Locate every leukocyte (white blood cell).
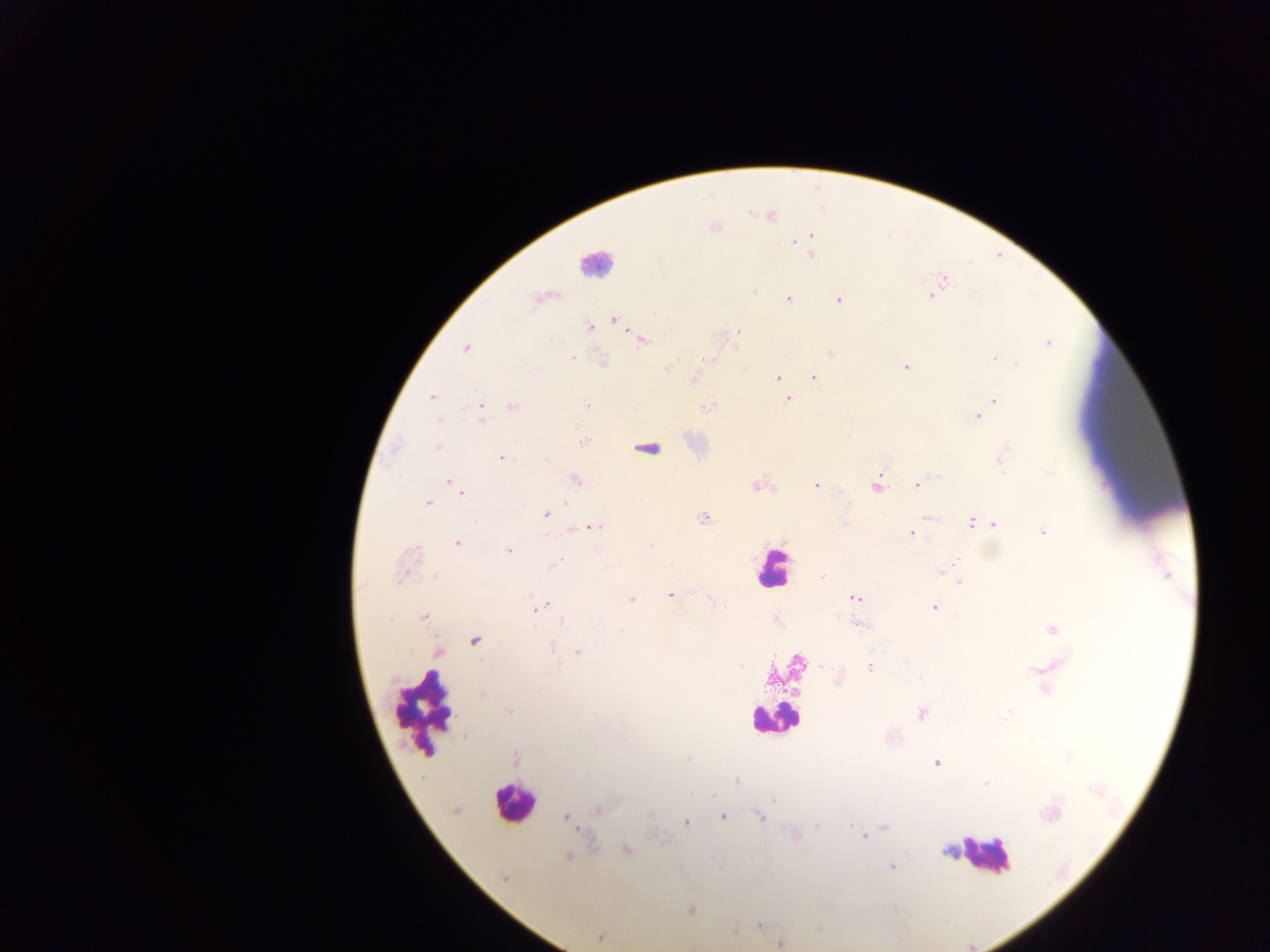

Approximate centers as x y in pixels.
Leukocytes: 595 263; 648 448; 773 569; 426 708; 773 718; 512 802; 984 854.

{
  "field_of_view": "single",
  "country": "Ghana",
  "malaria_parasite_locations": "approximate centers as x y in pixels: 771 216; 811 235; 802 239; 795 241; 812 255; 944 279; 754 291; 931 295; 788 298; 839 299; 615 321; 591 327; 738 331; 642 340; 1048 343; 465 349; 830 353; 572 358; 709 358; 993 358; 1017 364; 906 366; 666 369; 814 377; 777 378; 695 379; 431 397; 788 399; 996 400; 513 405; 587 405; 708 407; 482 415; 977 415; 439 420; 584 442; 438 446; 1001 457; 501 458; 1051 473; 575 479; 448 481; 876 484; 756 485; 816 485; 916 485; 462 493; 428 502; 566 503; 545 515; 927 517; 703 518; 972 521; 994 524; 845 525; 594 527; 1043 532; 912 533; 457 542; 651 545; 414 551; 508 551; 555 564; 941 571; 823 576; 948 576; 402 577; 960 582; 482 584; 670 594; 855 597; 632 600; 545 604; 934 607; 539 608; 724 608; 423 617; 562 621; 859 624; 1052 629; 475 640; 551 647; 578 652; 439 653; 871 668; 841 672; 481 695; 922 714; 1007 714; 515 758; 937 763; 737 780; 714 794; 774 799; 599 810; 1049 815; 759 816; 566 817; 723 817; 686 822; 817 825; 850 825; 885 827; 864 837; 626 849; 568 857; 891 866; 504 878; 691 910; 760 926; 600 938; 780 944",
  "capture": "mobile-phone photograph through a microscope",
  "image_size": "1270×952 pixels",
  "preparation": "thick blood smear"
}